Outline each blood parasite and name the species.
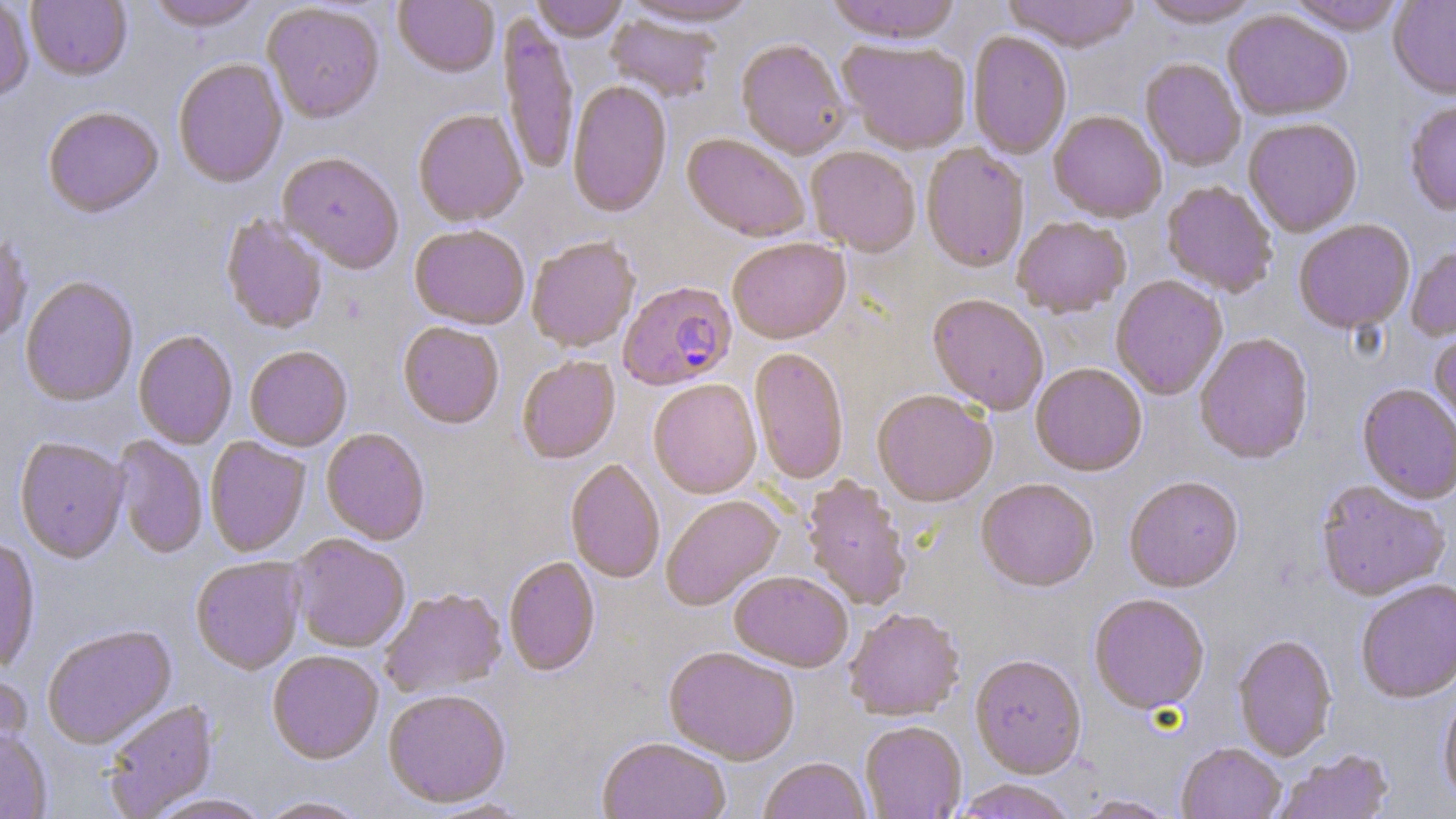
Approximate bounding boxes as (x1,y1)-(x2,y2) corner pairs in pixels.
Plasmodium falciparum-infected red blood cells: (618,281)-(737,392).
No Plasmodium ovale, Plasmodium malariae, Plasmodium vivax, Babesia divergens, or Trypanosoma brucei observed.

Summary:
  - Uninfected red blood cell locations: (25,0)-(132,82), (145,0)-(263,32), (393,0)-(499,80), (530,0)-(629,43), (619,0)-(760,28), (825,0)-(962,44), (1002,0)-(1142,52), (1139,0)-(1262,28), (1286,0)-(1406,36), (1388,0)-(1456,100), (0,1)-(33,103), (262,4)-(385,126), (1222,9)-(1353,121), (605,14)-(720,103), (498,15)-(578,176), (967,30)-(1072,159), (838,40)-(972,154), (736,41)-(850,160), (1140,58)-(1246,171), (173,60)-(288,190), (567,82)-(672,219), (1405,100)-(1456,217), (43,108)-(163,219), (412,110)-(527,228), (1048,110)-(1166,222), (1243,118)-(1363,237), (682,134)-(809,243), (920,143)-(1030,273), (806,147)-(920,256), (277,154)-(403,275), (1161,180)-(1278,298), (1012,215)-(1131,317), (221,216)-(327,335), (1293,219)-(1415,334), (409,227)-(529,331), (0,233)-(32,347), (526,238)-(640,353), (728,238)-(851,345), (1405,244)-(1456,342), (1111,275)-(1228,400), (21,277)-(139,408), (927,294)-(1049,415), (398,323)-(504,430), (1429,329)-(1456,436), (133,331)-(237,449), (1194,333)-(1314,464), (245,347)-(352,452), (749,348)-(849,486), (517,356)-(620,465), (1030,363)-(1147,476), (648,381)-(762,499), (1357,384)-(1456,504), (872,390)-(997,508), (321,429)-(430,546), (111,436)-(207,559), (205,437)-(311,558), (14,438)-(129,564), (565,460)-(665,584), (802,476)-(912,611), (1124,476)-(1243,593), (975,480)-(1099,593), (1316,481)-(1450,602), (661,495)-(784,611), (289,535)-(410,654), (0,539)-(40,672), (190,557)-(306,675), (504,558)-(600,676), (729,572)-(853,672), (1355,579)-(1456,703), (379,589)-(507,699), (1089,595)-(1210,715), (844,609)-(964,722), (42,626)-(177,750), (1232,635)-(1338,761), (663,647)-(799,766), (267,652)-(383,765), (970,656)-(1086,779), (0,670)-(32,767), (1438,686)-(1456,808), (383,690)-(511,809), (103,699)-(218,817), (860,722)-(966,819), (0,730)-(52,818), (596,738)-(731,819), (1177,743)-(1285,819), (1273,749)-(1394,819), (758,758)-(871,819), (951,780)-(1078,819), (147,794)-(271,819), (1073,795)-(1180,818), (256,797)-(370,818)
  - Slide-level diagnosis: Plasmodium falciparum
  - Magnification: 1000x
  - Modality: light microscopy
  - Stain: May-Grünwald-Giemsa
  - Preparation: thin blood film
  - Image size: 1456×819 pixels
  - Field of view: single